Name the blood parasite species.
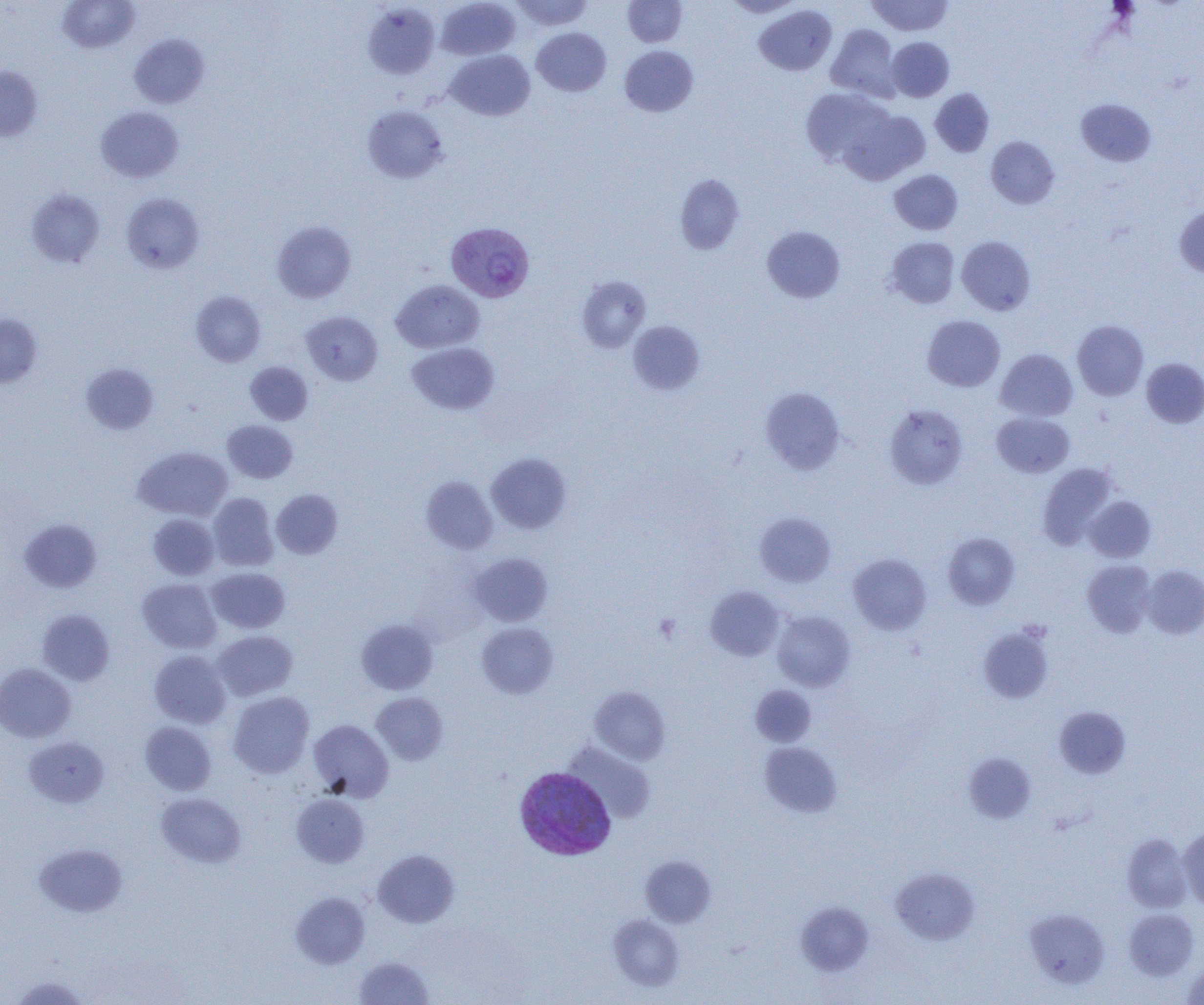

Plasmodium vivax.

Summary:
  - Coordinate format: approximate bounding boxes as (x1, y1, x2, y2) in pixels
  - Plasmodium vivax-infected red blood cell locations: (445, 222, 535, 302), (515, 767, 616, 861)
  - Platelet locations: (654, 614, 681, 641)
  - Uninfected red blood cell locations: (57, 0, 140, 53), (436, 0, 520, 60), (511, 0, 594, 30), (623, 0, 687, 47), (724, 0, 802, 17), (866, 0, 953, 36), (362, 3, 440, 79), (754, 5, 837, 76), (826, 24, 900, 100), (531, 27, 611, 96), (129, 34, 210, 108), (887, 37, 954, 102), (619, 45, 698, 117), (446, 49, 535, 121), (0, 66, 43, 142), (800, 87, 895, 168), (930, 89, 994, 157), (1076, 98, 1157, 167), (362, 105, 449, 184), (95, 106, 183, 182), (840, 107, 930, 185), (986, 136, 1059, 209), (889, 169, 963, 235), (675, 174, 745, 254), (25, 188, 105, 268), (121, 193, 204, 273), (1174, 206, 1204, 278), (272, 220, 357, 303), (762, 226, 845, 303), (957, 236, 1036, 315), (885, 237, 960, 308), (576, 275, 651, 353), (391, 280, 484, 353), (191, 290, 266, 367), (301, 311, 382, 385), (0, 314, 42, 388), (922, 315, 1005, 392), (628, 320, 705, 394), (1073, 320, 1149, 400), (407, 342, 499, 415), (995, 348, 1078, 422), (1141, 358, 1204, 428), (245, 361, 313, 425), (80, 362, 159, 435), (761, 387, 845, 475), (884, 404, 969, 489), (991, 412, 1075, 477), (222, 420, 298, 484), (133, 446, 233, 521), (486, 452, 572, 534), (1037, 463, 1117, 549), (421, 476, 498, 554), (271, 489, 343, 559), (208, 492, 279, 571), (1085, 496, 1156, 562), (754, 512, 835, 587), (148, 514, 219, 581), (19, 518, 102, 593), (943, 532, 1019, 609), (469, 552, 552, 626), (848, 554, 931, 634), (1082, 560, 1157, 637), (1142, 565, 1204, 639), (206, 567, 290, 634), (137, 578, 222, 653), (705, 586, 785, 661), (37, 608, 115, 686), (772, 610, 855, 691), (356, 618, 438, 694), (476, 622, 558, 698), (979, 625, 1054, 704), (212, 630, 297, 700), (149, 650, 231, 728), (0, 662, 76, 743), (750, 684, 816, 746), (589, 686, 670, 765), (227, 691, 314, 778), (372, 692, 448, 765), (1054, 706, 1131, 778), (309, 719, 394, 802), (139, 721, 216, 795), (24, 736, 109, 807), (760, 741, 842, 817), (562, 742, 655, 824), (964, 752, 1036, 823), (156, 793, 246, 868), (291, 793, 370, 867), (1178, 827, 1204, 908), (1122, 833, 1192, 912), (35, 843, 127, 917), (372, 849, 459, 927), (640, 856, 716, 927), (891, 867, 980, 944), (290, 892, 370, 968), (796, 902, 873, 976), (1025, 908, 1110, 988), (1124, 909, 1199, 980), (608, 914, 685, 992), (354, 956, 434, 1004), (1182, 962, 1204, 1004), (10, 975, 92, 1005)
  - Modality: optical microscopy
  - Image size: 1204×1005 pixels
  - Preparation: thin blood smear
  - Magnification: 1000x
  - Field of view: one of a larger specimen